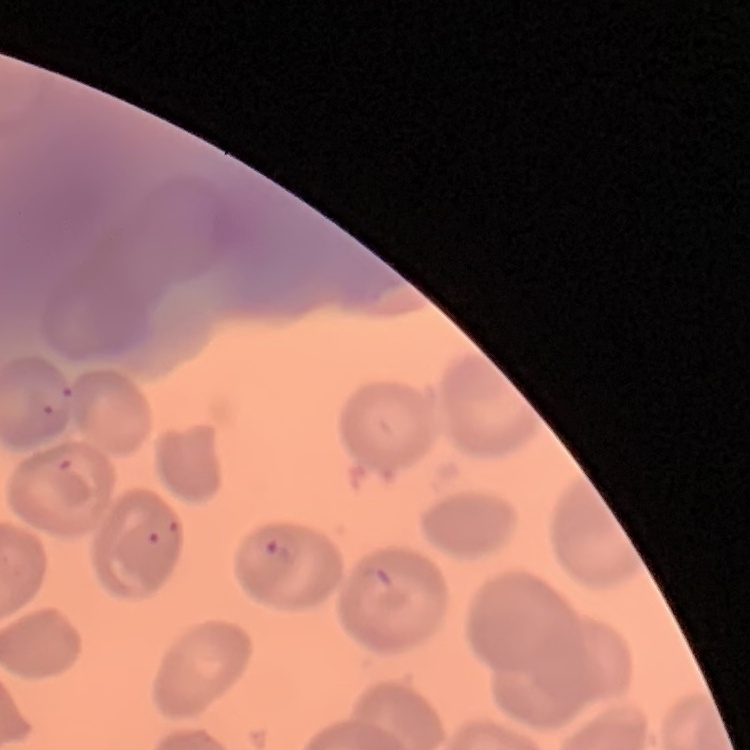

The erythrocytes show no rouleaux formation. One tile cut from a larger photomicrograph. Thin blood smear. Field's or Giemsa stain.